Assess this cell for malaria.
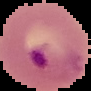

Parasitized.

Summary:
  - Preparation: thin blood smear
  - Image size: 91×91 pixels
  - Image type: segmented cell region on a black background